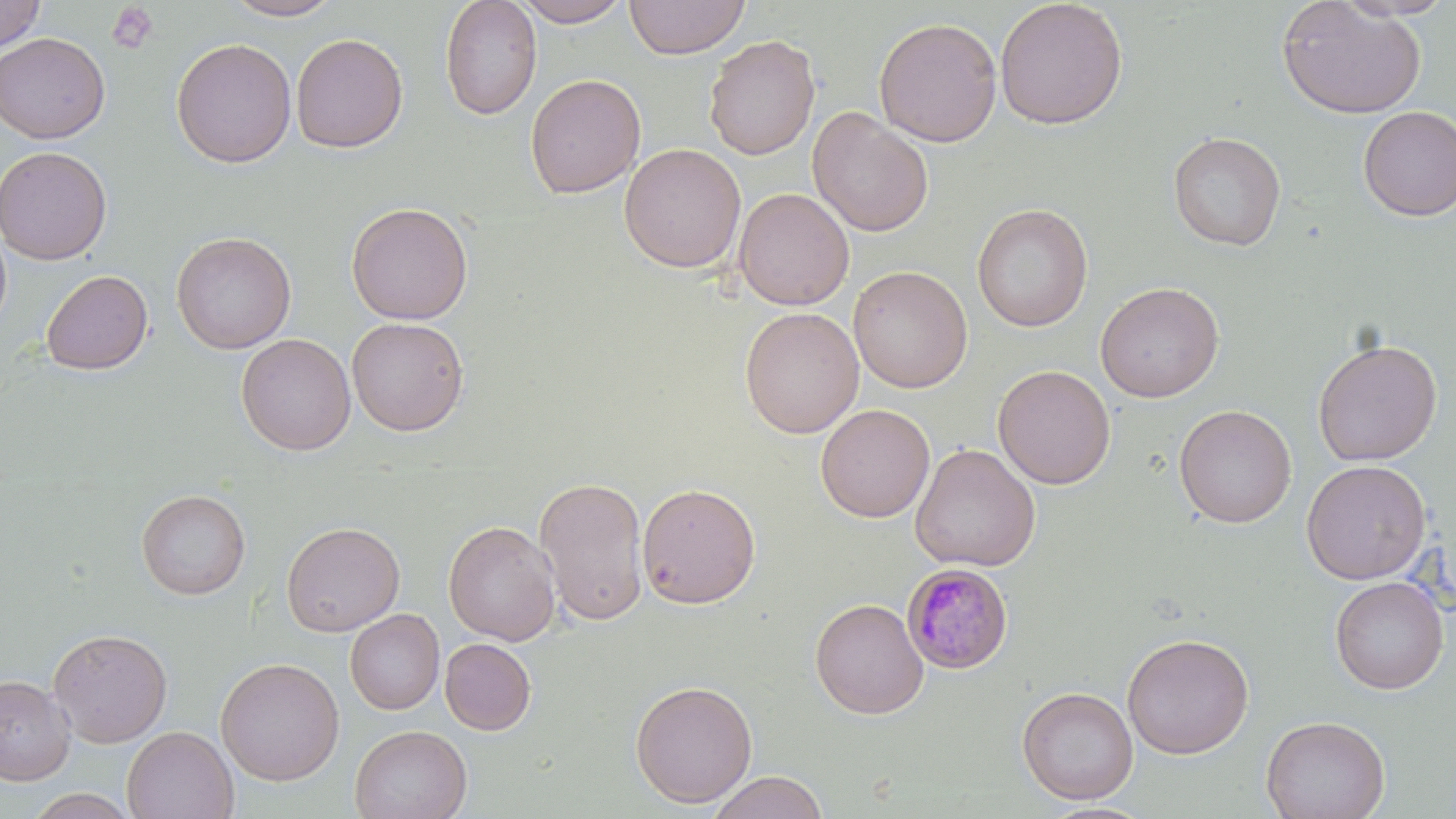

Summary:
  - Coordinate format: approximate bounding boxes as (x1,y1)-(x2,y2) corner pairs in pixels
  - Platelet locations: (106,2)-(160,55)
  - Uninfected red blood cell locations: (221,0)-(344,21), (439,0)-(542,121), (512,0)-(633,27), (624,0)-(750,59), (994,0)-(1129,130), (1276,0)-(1427,120), (1333,0)-(1454,21), (0,1)-(47,53), (873,16)-(1002,147), (0,32)-(111,144), (290,33)-(409,153), (703,34)-(820,161), (171,38)-(297,168), (524,73)-(646,199), (1357,106)-(1456,222), (807,107)-(934,238), (1167,131)-(1287,251), (619,144)-(746,274), (0,145)-(113,265), (734,188)-(855,311), (346,202)-(473,325), (972,203)-(1093,332), (0,221)-(12,335), (171,231)-(297,355), (848,265)-(973,393), (41,270)-(153,376), (1095,281)-(1225,402), (740,307)-(865,438), (346,316)-(469,436), (236,333)-(356,456), (1312,338)-(1442,466), (992,365)-(1116,490), (815,403)-(935,523), (1174,404)-(1296,528), (910,443)-(1041,572), (1301,460)-(1431,585), (534,476)-(649,626), (637,481)-(761,609), (136,488)-(251,599), (443,520)-(561,646), (281,521)-(405,637), (1329,576)-(1449,694), (809,598)-(929,719), (345,609)-(444,714), (47,627)-(173,748), (1121,632)-(1255,759), (439,638)-(536,735), (215,657)-(345,786), (0,675)-(75,784), (629,679)-(758,808), (1016,686)-(1139,805), (1260,714)-(1391,819), (350,724)-(472,819), (122,726)-(238,818), (708,770)-(828,819), (28,788)-(139,819), (1038,801)-(1156,819)
  - Plasmodium malariae-infected red blood cell locations: (901,563)-(1014,674)
  - Slide-level diagnosis: Plasmodium malariae
  - Magnification: 1000x
  - Field of view: one of a larger specimen
  - Modality: light microscopy
  - Stain: May-Grünwald-Giemsa
  - Image size: 1456×819 pixels
  - Preparation: thin blood film